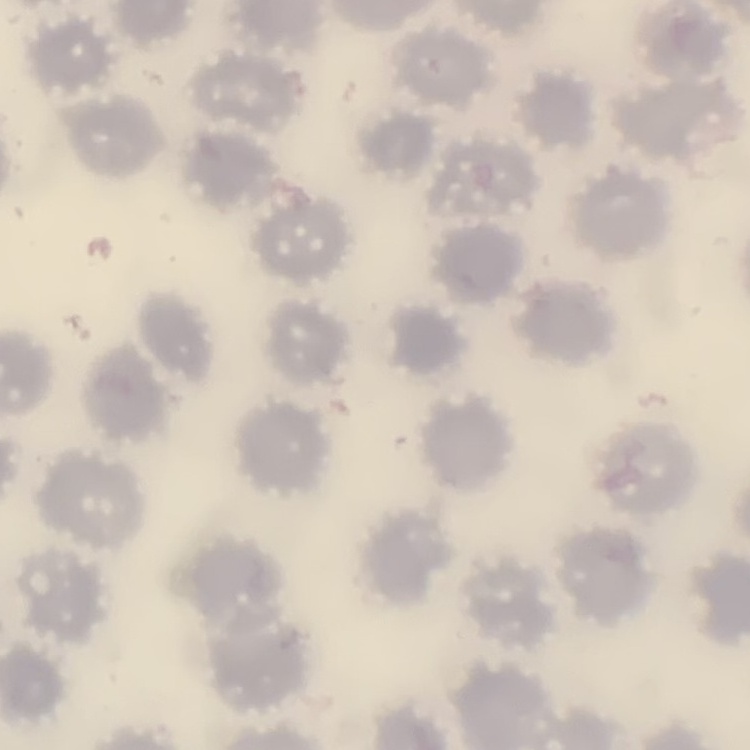
red_blood_cell_morphology: no rouleaux formation
stain: Field's or Giemsa
image_type: one tile cut from a larger photomicrograph
preparation: thin peripheral smear